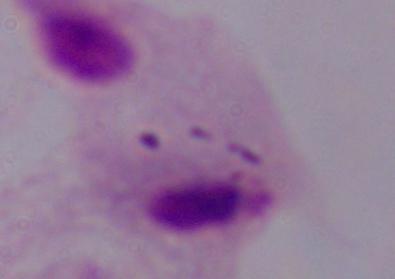
modality = photomicrograph
magnification = 1000x
identification = trichomonad